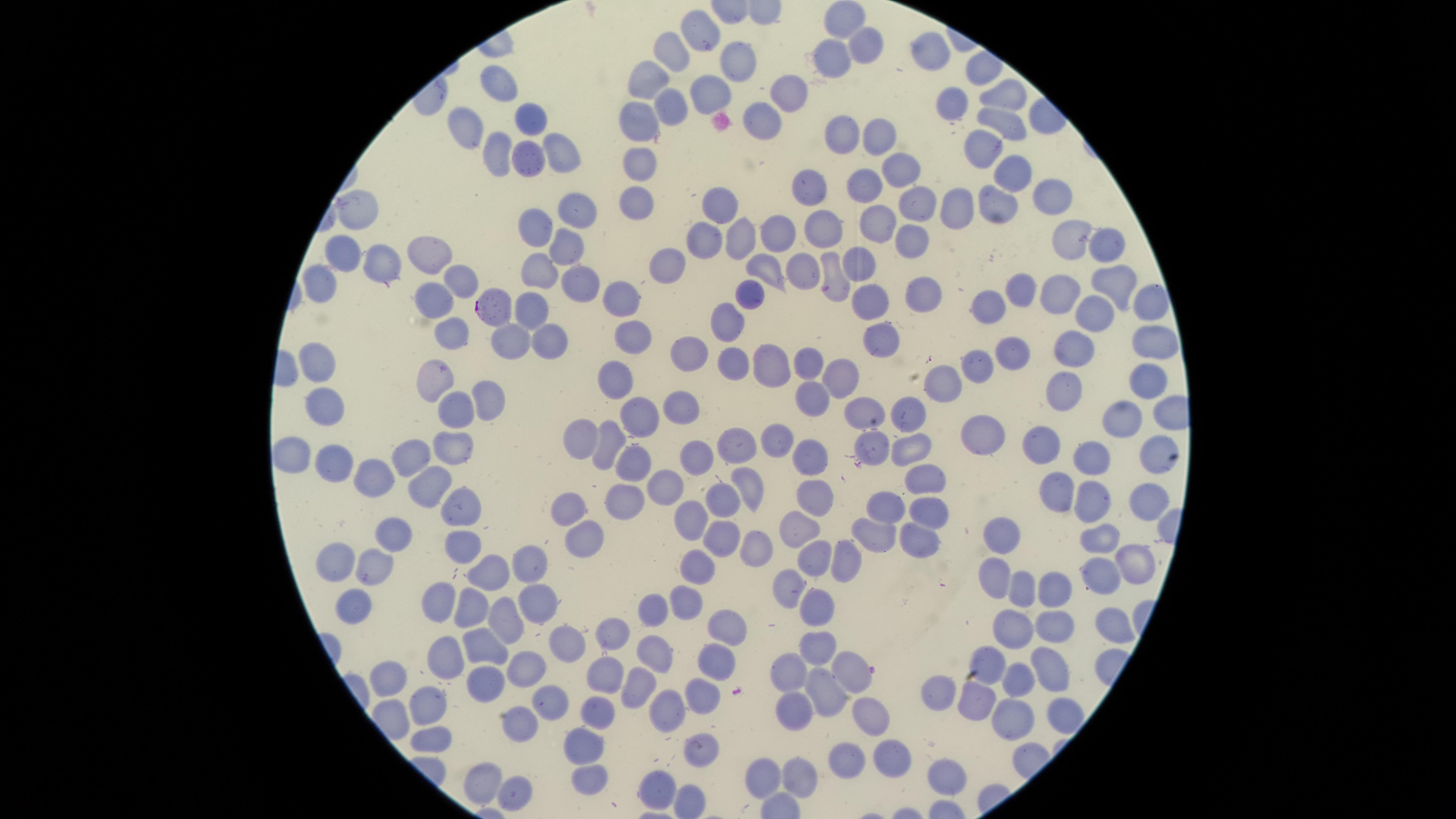

Approximate marker points as {x, y} in pixels. Uninfected red blood cells: {844, 21}, {702, 30}, {865, 43}, {931, 49}, {669, 53}, {737, 57}, {834, 66}, {496, 80}, {654, 84}, {706, 87}, {1006, 93}, {951, 97}, {788, 100}, {669, 104}, {534, 116}, {1010, 116}, {642, 118}, {764, 119}, {466, 129}, {846, 130}, {880, 138}, {559, 143}, {984, 148}, {501, 149}, {534, 154}, {643, 158}, {899, 165}, {1010, 171}, {865, 183}, {810, 192}, {1048, 195}, {636, 199}, {912, 206}, {997, 206}, {563, 207}, {716, 213}, {957, 213}, {353, 215}, {537, 224}, {824, 225}, {875, 225}, {784, 230}, {1074, 235}, {735, 239}, {908, 240}, {702, 242}, {1108, 242}, {569, 245}, {346, 255}, {428, 257}, {803, 263}, {383, 264}, {859, 264}, {773, 266}, {545, 268}, {831, 269}, {667, 270}, {455, 273}, {581, 281}, {1119, 284}, {324, 287}, {1023, 290}, {436, 295}, {754, 295}, {926, 297}, {871, 299}, {623, 301}, {1060, 302}, {538, 304}, {988, 305}, {1147, 306}, {729, 315}, {1099, 315}, {452, 330}, {629, 331}, {546, 337}, {882, 341}, {1156, 343}, {507, 346}, {1069, 346}, {685, 353}, {1015, 353}, {731, 366}, {771, 366}, {806, 366}, {972, 368}, {328, 372}, {842, 374}, {618, 376}, {1143, 377}, {430, 383}, {940, 388}, {1064, 388}, {811, 396}, {484, 397}, {329, 402}, {670, 405}, {861, 407}, {450, 410}, {1119, 412}, {634, 413}, {915, 419}, {589, 430}, {979, 436}, {768, 437}, {870, 440}, {1041, 440}, {452, 442}, {604, 445}, {731, 448}, {906, 450}, {1091, 450}, {1151, 450}, {287, 451}, {413, 454}, {688, 460}, {806, 460}, {333, 461}, {623, 463}, {381, 473}, {925, 474}, {746, 483}, {434, 484}, {661, 486}, {1053, 487}, {819, 490}, {720, 493}, {1146, 496}, {621, 503}, {890, 503}, {1093, 503}, {462, 505}, {926, 506}, {571, 509}, {691, 521}, {802, 526}, {586, 531}, {878, 533}, {388, 534}, {917, 537}, {1093, 538}, {458, 539}, {1005, 539}, {716, 544}, {761, 548}, {342, 558}, {813, 559}, {840, 560}, {1131, 560}, {534, 567}, {374, 568}, {697, 572}, {1099, 573}, {484, 576}, {993, 578}, {791, 586}, {1051, 589}, {1020, 590}, {439, 595}, {538, 598}, {359, 602}, {686, 605}, {472, 607}, {813, 609}, {658, 614}, {511, 616}, {1118, 626}, {729, 627}, {1018, 627}, {1052, 629}, {610, 633}, {570, 640}, {482, 646}, {813, 646}, {654, 653}, {709, 657}, {1000, 659}, {439, 661}, {852, 667}, {524, 669}, {606, 669}, {796, 669}, {490, 670}, {1051, 671}, {1023, 674}, {391, 678}, {640, 681}, {830, 688}, {702, 689}, {943, 694}, {980, 701}, {428, 704}, {667, 704}, {792, 706}, {554, 709}, {1060, 711}, {596, 713}, {1007, 719}, {867, 722}, {511, 726}, {433, 734}, {584, 745}, {702, 748}, {847, 757}, {890, 758}, {589, 771}, {764, 774}, {799, 774}, {945, 775}, {476, 783}, {659, 783}, {516, 790}. Parasitized red blood cells: {496, 305}. Thin smear of blood. Single field of view. Circular visible region. Photographed with a smartphone camera through the microscope eyepiece. Giemsa-stained preparation. Presence: malaria parasites detected. Image is 1456×819 pixels. Species: Plasmodium falciparum.